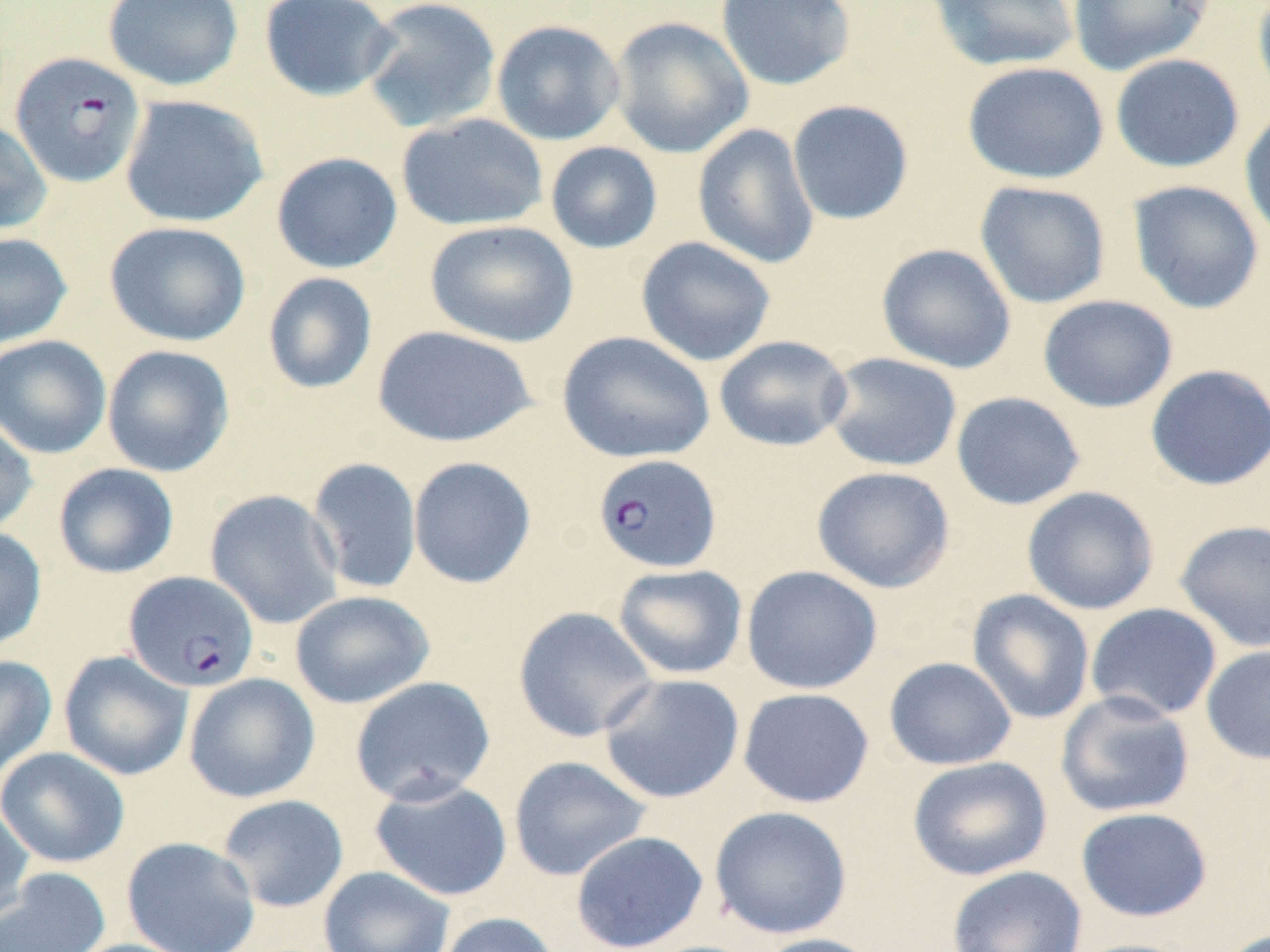

slide-level diagnosis = Plasmodium falciparum
preparation = thin blood film
uninfected red blood cell locations = approximate bounding boxes as (x1, y1, x2, y2) in pixels: (102, 0, 244, 91), (258, 0, 398, 102), (360, 0, 502, 134), (715, 0, 857, 91), (925, 0, 1081, 72), (1067, 0, 1216, 75), (1252, 0, 1270, 108), (609, 16, 753, 158), (490, 19, 626, 146), (1111, 53, 1245, 173), (962, 61, 1110, 184), (120, 95, 269, 228), (787, 100, 914, 225), (1239, 105, 1270, 247), (396, 113, 548, 232), (0, 119, 52, 235), (692, 123, 820, 270), (545, 141, 663, 254), (271, 151, 403, 274), (974, 180, 1111, 309), (1128, 180, 1265, 314), (424, 219, 579, 347), (104, 221, 251, 347), (0, 232, 72, 348), (635, 236, 777, 367), (876, 243, 1016, 373), (262, 271, 378, 395), (1038, 294, 1178, 413), (371, 325, 537, 448), (557, 330, 715, 464), (0, 335, 112, 459), (714, 335, 853, 452), (102, 344, 235, 477), (822, 352, 962, 472), (1145, 364, 1270, 491), (951, 391, 1086, 510), (0, 415, 38, 537), (408, 456, 537, 589), (307, 457, 422, 596), (53, 463, 179, 578), (812, 466, 955, 593), (1021, 486, 1159, 615), (205, 489, 344, 629), (1174, 519, 1270, 652), (0, 525, 47, 652), (612, 564, 747, 679), (741, 565, 883, 695), (966, 589, 1095, 725), (290, 590, 435, 709), (1085, 603, 1223, 722), (512, 606, 660, 742), (1201, 644, 1270, 765), (58, 650, 193, 781), (0, 654, 57, 785), (883, 656, 1017, 770), (184, 673, 320, 803), (598, 673, 745, 804), (350, 676, 496, 806), (738, 687, 875, 808), (1055, 691, 1195, 818), (0, 747, 130, 868), (508, 756, 651, 882), (907, 756, 1053, 881), (369, 777, 513, 902), (217, 794, 349, 913), (0, 802, 35, 924), (709, 805, 852, 940), (1075, 807, 1213, 922), (570, 830, 709, 952), (121, 836, 261, 952), (318, 865, 455, 952), (947, 865, 1087, 952), (0, 867, 111, 952), (437, 912, 562, 952), (752, 933, 884, 952), (61, 938, 203, 952), (1064, 938, 1200, 952)
Plasmodium falciparum-infected red blood cell locations = approximate bounding boxes as (x1, y1, x2, y2) in pixels: (11, 51, 147, 188), (592, 453, 721, 573), (124, 571, 258, 692)
image size = 1270×952 pixels
stain = May-Grünwald-Giemsa
magnification = 1000x
modality = light microscopy
field of view = single